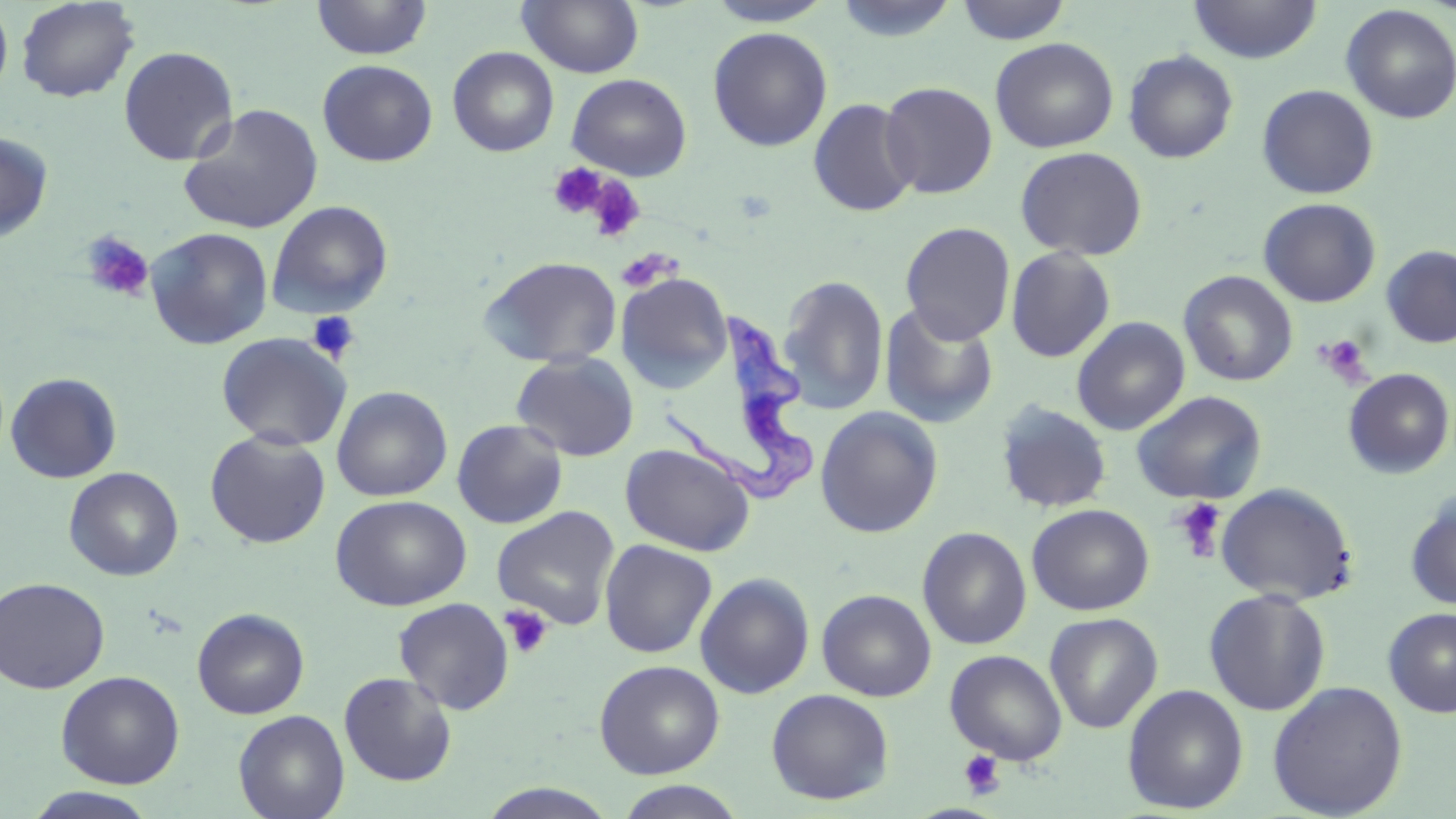
Approximate bounding boxes as (x1,y1)-(x2,y2) corner pairs in pixels. Platelet locations: (548,162)-(608,219), (585,176)-(646,243), (79,230)-(154,303), (616,248)-(678,292), (307,310)-(361,364), (1316,335)-(1372,384), (1170,498)-(1228,562), (500,605)-(553,659), (959,750)-(1005,799). Trypanosoma brucei locations: (668,308)-(825,507). Uninfected red blood cell locations: (16,0)-(140,103), (311,0)-(432,60), (703,0)-(836,27), (833,0)-(961,43), (955,0)-(1073,45), (1188,0)-(1322,63), (517,1)-(644,78), (0,2)-(14,102), (1340,4)-(1456,124), (708,26)-(833,151), (990,37)-(1119,153), (118,45)-(239,166), (447,46)-(560,157), (1123,49)-(1238,163), (317,60)-(438,166), (565,73)-(693,181), (879,81)-(998,198), (1257,84)-(1379,199), (807,97)-(920,217), (179,104)-(324,234), (0,130)-(54,244), (1015,146)-(1148,261), (1258,198)-(1381,308), (266,200)-(393,319), (900,222)-(1016,345), (145,227)-(273,349), (1381,245)-(1456,348), (1005,246)-(1115,363), (478,256)-(623,368), (1178,270)-(1298,387), (616,272)-(733,392), (778,274)-(889,415), (879,302)-(1000,428), (1072,316)-(1191,435), (216,332)-(352,451), (511,352)-(639,462), (1343,368)-(1455,479), (5,372)-(122,483), (332,385)-(452,502), (1132,391)-(1267,504), (994,401)-(1113,513), (814,406)-(943,538), (452,419)-(568,529), (205,429)-(331,549), (620,443)-(755,556), (64,466)-(184,581), (1215,483)-(1358,605), (1405,493)-(1456,611), (330,495)-(472,611), (1027,504)-(1155,615), (492,505)-(621,630), (917,526)-(1032,650), (599,539)-(717,658), (695,572)-(815,699), (0,576)-(110,694), (817,588)-(937,701), (1203,588)-(1332,715), (393,597)-(515,714), (192,607)-(309,719), (1383,608)-(1456,718), (1044,612)-(1163,733), (944,649)-(1068,765), (594,659)-(724,779), (56,670)-(185,789), (338,671)-(458,786), (1267,680)-(1408,818), (1122,684)-(1249,814), (766,688)-(894,805), (233,709)-(350,819), (612,781)-(749,819), (22,787)-(161,819). Slide-level diagnosis: Trypanosoma brucei. May-Grünwald-Giemsa-stained preparation. 1000x magnification. Single field of view. Image is 1456×819 pixels. Thin blood film. Light microscopy.